Name the parasite shown.
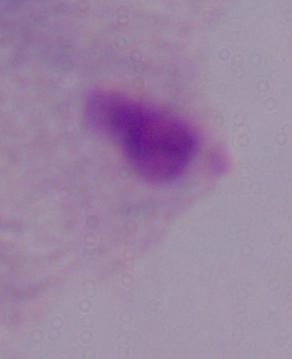

This is a trichomonad.

magnification = 1000x
modality = photomicrograph